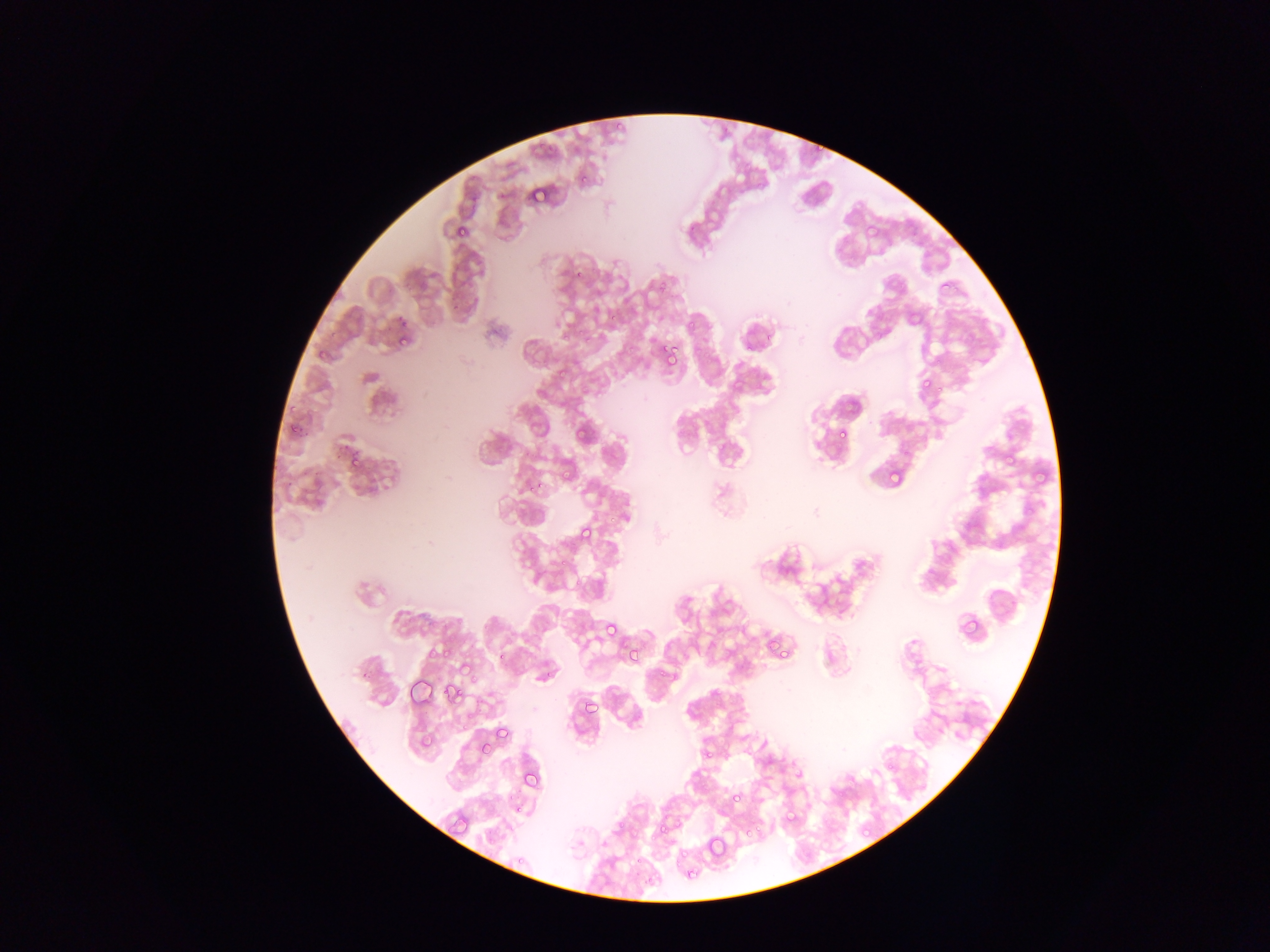

Approximate bounding boxes as {left, top, right, bottom} in pixels. Malaria parasite locations: {616, 121, 625, 133}, {807, 143, 823, 156}, {578, 171, 590, 186}, {530, 185, 548, 203}, {447, 215, 473, 237}, {572, 260, 589, 280}, {938, 277, 955, 293}, {656, 280, 668, 291}, {607, 312, 620, 323}, {908, 312, 918, 321}, {397, 316, 407, 326}, {682, 323, 698, 335}, {332, 328, 343, 339}, {558, 334, 568, 347}, {399, 335, 412, 352}, {742, 343, 755, 356}, {661, 345, 677, 362}, {920, 377, 933, 390}, {934, 381, 945, 398}, {288, 421, 305, 434}, {574, 424, 585, 439}, {835, 426, 848, 440}, {713, 439, 725, 452}, {1004, 445, 1020, 461}, {347, 452, 362, 473}, {560, 464, 571, 479}, {1032, 466, 1051, 483}, {887, 469, 902, 485}, {536, 476, 547, 489}, {523, 478, 538, 500}, {604, 508, 625, 524}, {578, 523, 595, 540}, {560, 536, 574, 549}, {552, 559, 565, 573}, {961, 614, 980, 635}, {604, 621, 618, 635}, {762, 642, 775, 650}, {782, 646, 792, 660}, {443, 647, 452, 658}, {626, 647, 640, 662}, {427, 651, 435, 664}, {495, 655, 506, 662}, {458, 657, 471, 674}, {468, 671, 482, 690}, {442, 682, 459, 700}, {580, 698, 597, 715}, {462, 710, 473, 727}, {499, 728, 514, 743}, {421, 736, 438, 745}, {477, 740, 489, 754}, {701, 748, 713, 760}, {523, 778, 544, 790}, {727, 786, 745, 808}, {515, 806, 526, 815}, {781, 811, 797, 826}, {671, 812, 687, 825}, {450, 818, 471, 836}, {656, 820, 669, 835}, {744, 824, 764, 844}, {862, 824, 872, 836}, {706, 833, 727, 857}, {678, 847, 698, 863}, {628, 848, 644, 871}, {635, 868, 654, 896}, {688, 868, 703, 877}. Image is 1270×952 pixels. Thin blood smear. Sample from Ghana. Single field of view. Photographed through a microscope with a mobile-phone camera.